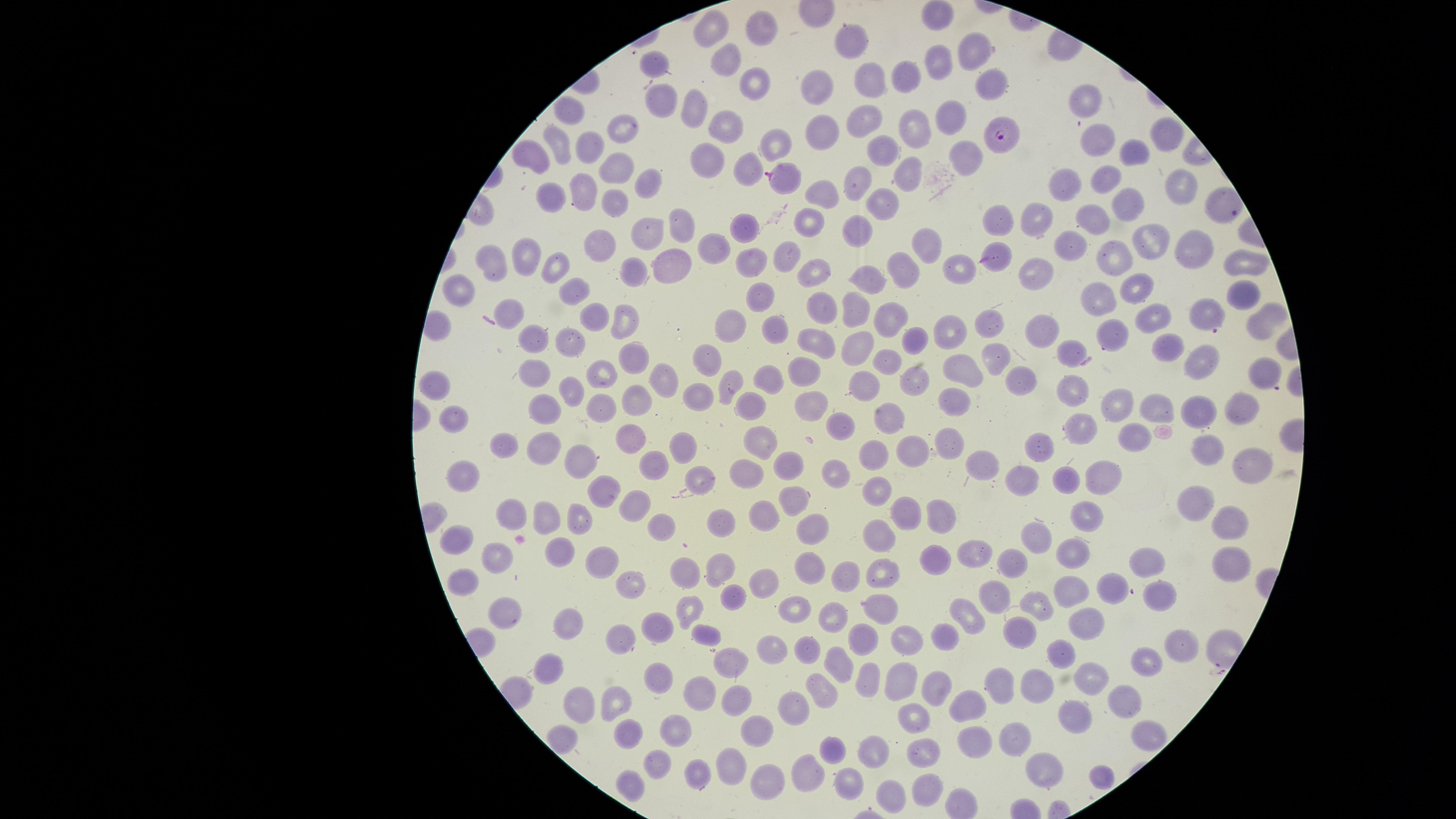
Approximate marker points as {x, y} in pixels. Parasitized red blood cells: {1000, 136}, {784, 175}, {993, 259}, {1207, 317}, {1266, 374}, {798, 498}. Uninfected red blood cells: {939, 12}, {760, 31}, {709, 33}, {851, 37}, {975, 51}, {654, 60}, {734, 63}, {939, 65}, {992, 80}, {869, 81}, {754, 83}, {906, 85}, {824, 92}, {663, 99}, {1088, 101}, {693, 109}, {570, 111}, {949, 115}, {861, 117}, {723, 123}, {915, 127}, {623, 128}, {828, 131}, {1166, 134}, {558, 142}, {1094, 142}, {782, 145}, {586, 146}, {885, 152}, {531, 153}, {962, 154}, {1127, 155}, {707, 157}, {616, 164}, {742, 167}, {909, 169}, {1105, 177}, {1178, 180}, {855, 181}, {1065, 185}, {580, 186}, {646, 186}, {549, 193}, {824, 195}, {611, 201}, {877, 203}, {1123, 206}, {1085, 218}, {1003, 219}, {1035, 219}, {806, 223}, {681, 227}, {860, 228}, {643, 229}, {743, 232}, {920, 240}, {1145, 242}, {597, 244}, {1062, 244}, {710, 248}, {1196, 248}, {789, 253}, {524, 254}, {671, 259}, {752, 260}, {1111, 260}, {493, 261}, {558, 262}, {953, 262}, {1243, 263}, {908, 270}, {813, 272}, {631, 273}, {1035, 276}, {870, 278}, {1137, 289}, {459, 290}, {570, 291}, {1240, 291}, {757, 298}, {1099, 298}, {818, 303}, {852, 308}, {514, 314}, {625, 318}, {1148, 318}, {595, 319}, {879, 319}, {737, 320}, {992, 323}, {1036, 323}, {774, 326}, {1257, 327}, {948, 331}, {1111, 332}, {572, 338}, {910, 338}, {532, 340}, {818, 341}, {856, 344}, {1069, 352}, {1165, 352}, {707, 355}, {996, 357}, {634, 358}, {884, 361}, {956, 365}, {1204, 367}, {605, 371}, {802, 371}, {661, 376}, {761, 376}, {906, 376}, {1014, 377}, {731, 381}, {534, 383}, {860, 384}, {439, 388}, {1065, 388}, {573, 390}, {691, 396}, {635, 402}, {749, 403}, {1111, 404}, {956, 405}, {808, 406}, {1152, 407}, {543, 408}, {596, 408}, {1195, 408}, {1248, 409}, {893, 415}, {450, 418}, {843, 422}, {1081, 427}, {759, 439}, {633, 441}, {684, 446}, {915, 446}, {950, 446}, {1039, 446}, {1207, 449}, {511, 450}, {547, 451}, {660, 460}, {880, 460}, {579, 461}, {984, 461}, {789, 464}, {845, 467}, {1250, 467}, {747, 471}, {463, 474}, {1103, 475}, {700, 476}, {1067, 480}, {1023, 481}, {876, 488}, {607, 491}, {1197, 496}, {630, 506}, {761, 510}, {547, 514}, {904, 516}, {512, 517}, {943, 518}, {1085, 518}, {722, 520}, {1229, 521}, {660, 525}, {809, 528}, {879, 534}, {1033, 536}, {462, 543}, {561, 549}, {977, 551}, {1073, 551}, {502, 556}, {1151, 559}, {604, 560}, {1009, 560}, {934, 561}, {1227, 562}, {723, 567}, {808, 567}, {687, 571}, {850, 571}, {885, 571}, {630, 580}, {766, 583}, {1107, 583}, {465, 585}, {1069, 588}, {1163, 591}, {999, 592}, {731, 594}, {880, 603}, {693, 605}, {1038, 605}, {793, 608}, {503, 613}, {830, 618}, {666, 619}, {572, 623}, {971, 623}, {1089, 624}, {626, 631}, {703, 634}, {904, 638}, {1012, 638}, {857, 639}, {932, 639}, {1179, 642}, {776, 648}, {809, 650}, {1063, 652}, {1147, 658}, {726, 662}, {839, 668}, {554, 670}, {663, 674}, {1090, 674}, {868, 679}, {1044, 682}, {903, 685}, {929, 686}, {1000, 687}, {699, 690}, {818, 692}, {733, 693}, {977, 699}, {1122, 699}, {611, 700}, {581, 705}, {794, 711}, {640, 715}, {1078, 715}, {913, 716}, {751, 728}, {675, 729}, {630, 733}, {1147, 734}, {1020, 737}, {980, 742}, {830, 748}, {879, 754}, {922, 755}, {654, 764}, {1045, 764}, {731, 768}, {688, 770}, {809, 772}, {1099, 774}, {768, 779}, {633, 786}, {846, 786}, {926, 789}, {890, 793}. Giemsa-stained preparation. Image is 1456×819 pixels. Smartphone photograph through the microscope eyepiece. Circular visible region. Thin blood film. One field of view of the specimen. Species: Plasmodium falciparum. Presence: malaria parasites identified.